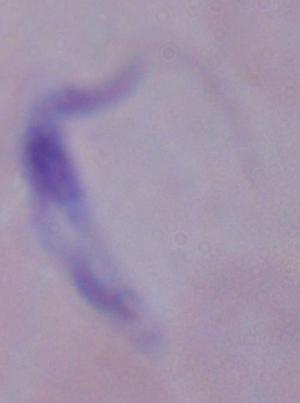

identification = trypanosome
modality = photomicrograph
magnification = 1000x